Report the malaria status of this cell.
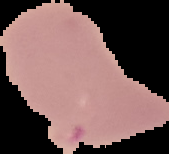

Uninfected.

From a thin blood film. Segmented cell region on a black background. Image is 169×154 pixels.